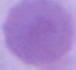 Micrograph. Captured at 1000x magnification. An erythrocyte is seen.